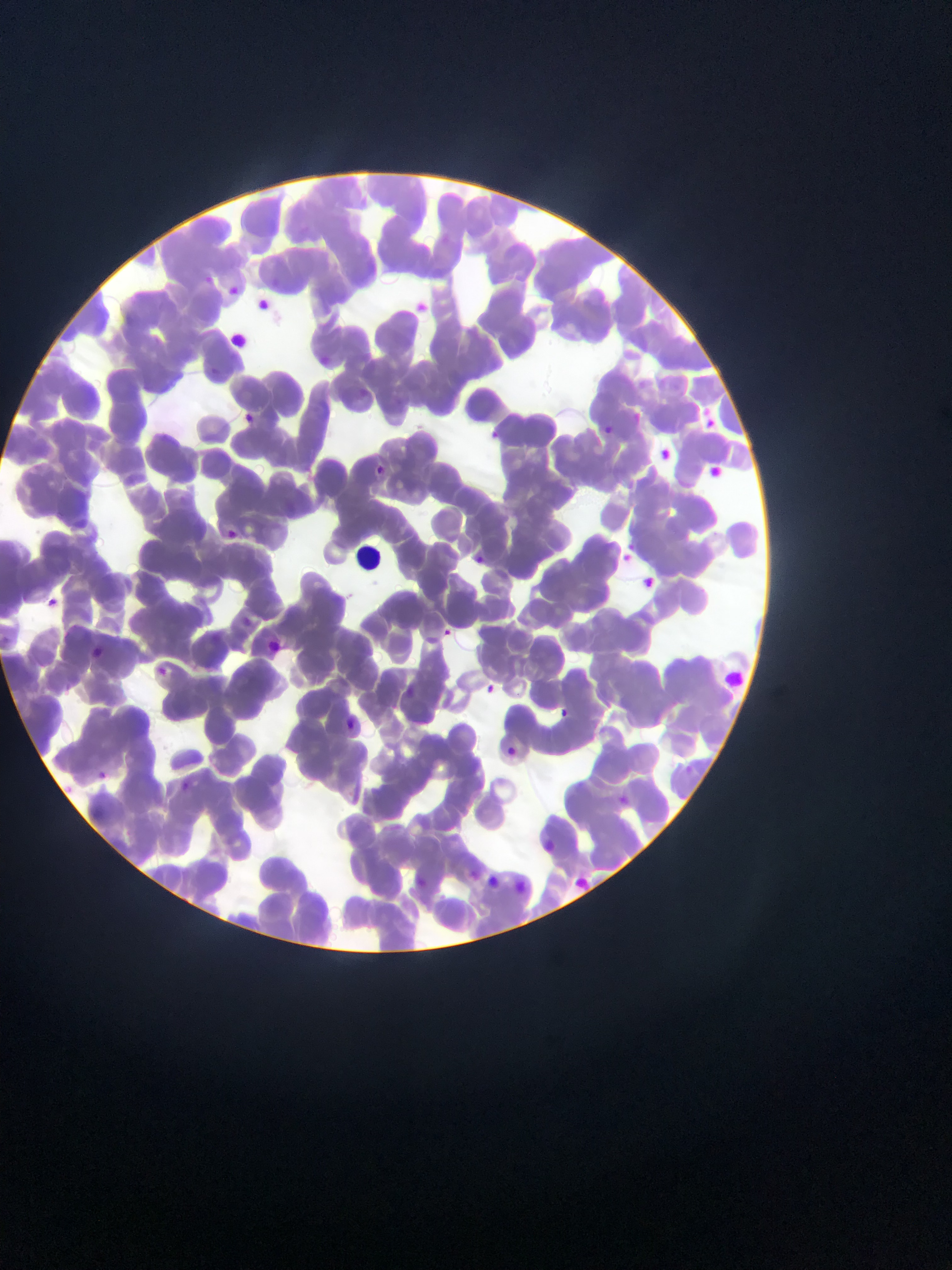

Approximate bounding boxes as [left, top, right, bottom] in pixels. Leukocyte locations: [349, 537, 379, 580]. Malaria parasite locations: [203, 270, 225, 298], [228, 280, 241, 302], [260, 295, 274, 312], [412, 297, 429, 316], [319, 352, 340, 368], [210, 362, 218, 378], [696, 403, 716, 425], [628, 406, 641, 423], [239, 410, 264, 429], [602, 423, 614, 441], [484, 427, 500, 441], [652, 445, 674, 465], [373, 459, 394, 481], [707, 462, 724, 476], [222, 520, 242, 548], [617, 546, 634, 568], [473, 547, 490, 570], [642, 571, 659, 588], [44, 595, 59, 605], [241, 615, 253, 632], [442, 627, 459, 646], [87, 644, 107, 662], [157, 663, 172, 678], [483, 682, 493, 694], [402, 683, 415, 695], [557, 701, 577, 718], [343, 715, 367, 735], [502, 745, 522, 761], [94, 765, 109, 780], [177, 777, 193, 791], [611, 786, 629, 803], [536, 836, 553, 849], [460, 868, 480, 882], [409, 872, 432, 892], [580, 872, 592, 891], [516, 876, 530, 894]. Single field of view. Photographed through a microscope with a mobile-phone camera. Thin blood smear. Image is 952×1270 pixels. Sample from Ghana.